Classify this cell by malaria status.
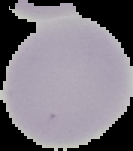
It is uninfected.

Summary:
  - Image size: 133×151 pixels
  - Image type: segmented cell region with the area outside set to black
  - Preparation: thin blood smear